Identify the parasite.
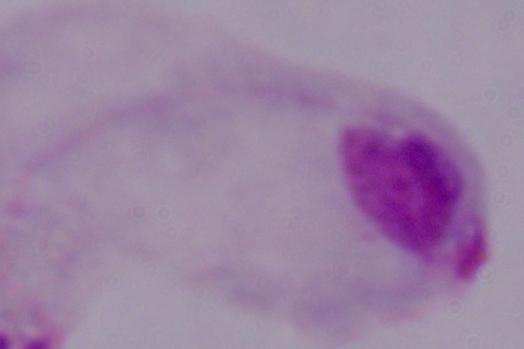

This is a trichomonad.

modality: micrograph
magnification: 1000x